Assess the morphology of the erythrocytes.
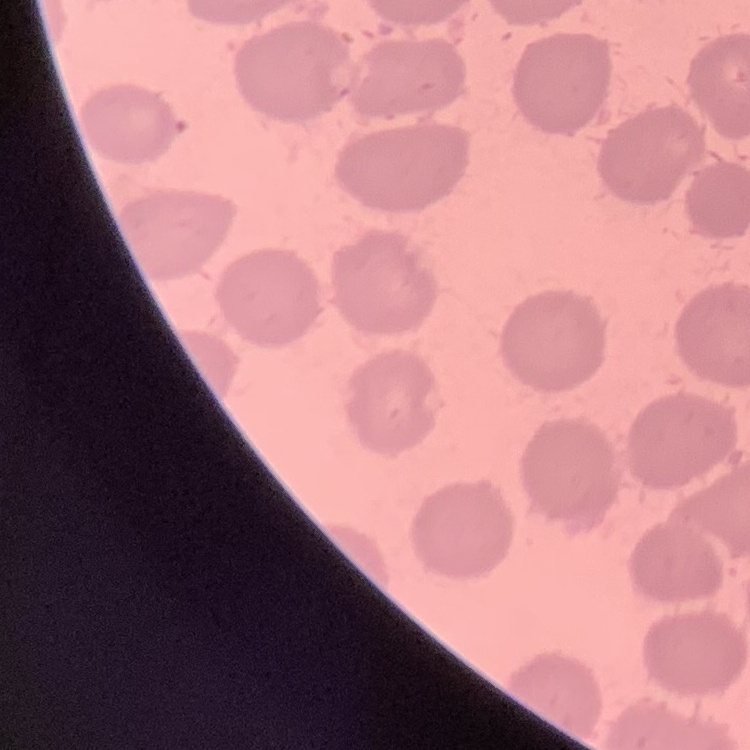

They show no rouleaux formation.

Thin blood smear. Field's or Giemsa stain. One tile cut from a larger photomicrograph.